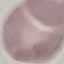
Result: no malaria parasites detected. Photographed with a smartphone camera at the microscope eyepiece. Automatically extracted cell patch, resized to 64 × 64 pixels. Thin blood smear. Giemsa stain.